Locate every blood parasite and identify its species.
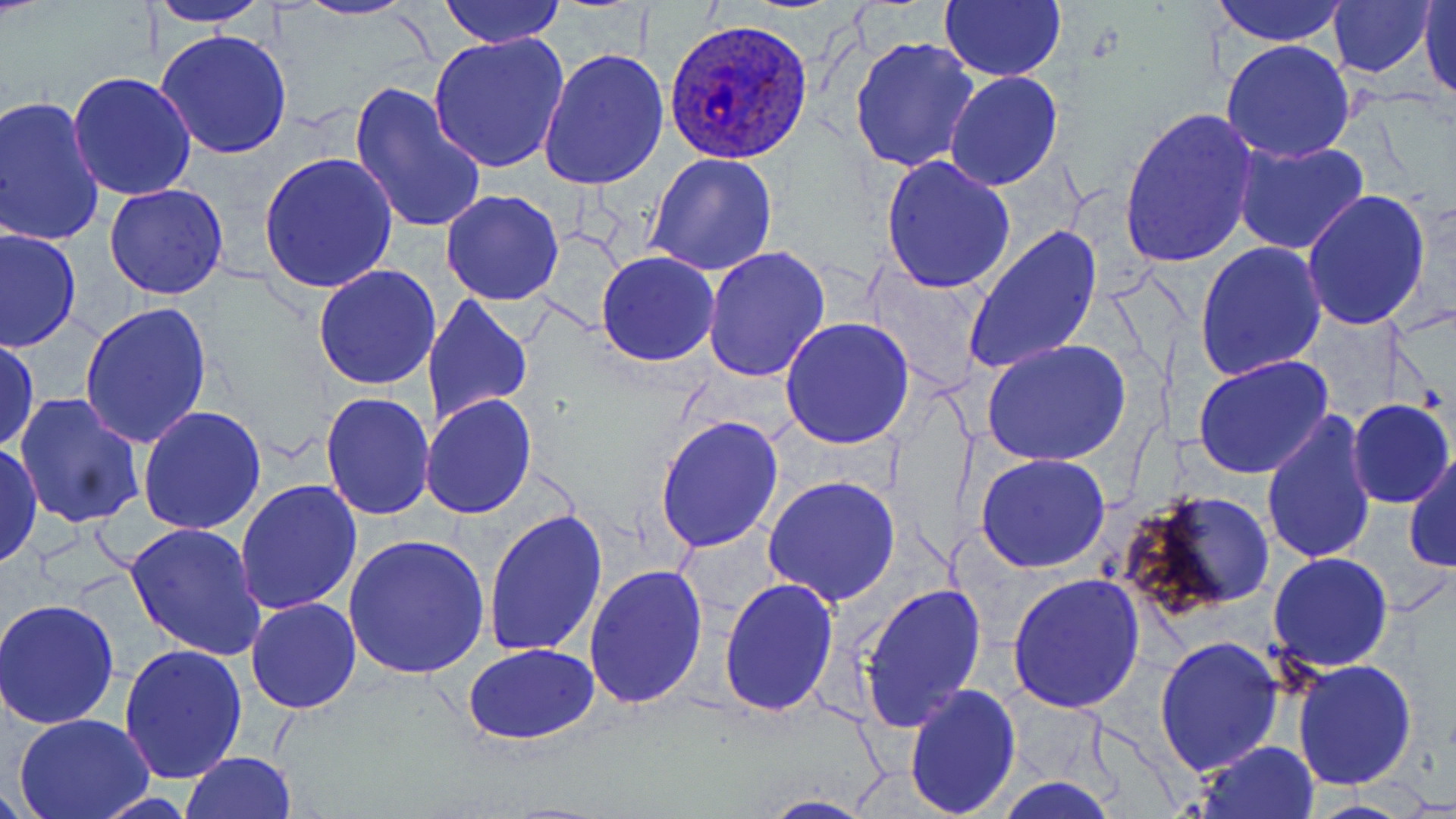

Approximate bounding boxes as named x1/y1/x2/y2 corners in pixels.
Plasmodium ovale-infected red blood cells: (x1=664, y1=21, x2=813, y2=165).
No Plasmodium falciparum, Plasmodium malariae, Plasmodium vivax, Babesia divergens, or Trypanosoma brucei observed.

slide-level diagnosis = Plasmodium ovale
modality = optical microscopy
magnification = 1000x
uninfected red blood cell locations = approximate bounding boxes as named x1/y1/x2/y2 corners in pixels: (x1=288, y1=0, x2=422, y2=21), (x1=436, y1=0, x2=569, y2=49), (x1=1208, y1=0, x2=1350, y2=48), (x1=147, y1=1, x2=272, y2=27), (x1=940, y1=2, x2=1066, y2=83), (x1=1418, y1=2, x2=1456, y2=100), (x1=1325, y1=3, x2=1438, y2=79), (x1=156, y1=29, x2=292, y2=159), (x1=429, y1=34, x2=569, y2=173), (x1=850, y1=36, x2=977, y2=175), (x1=1221, y1=41, x2=1355, y2=163), (x1=541, y1=48, x2=668, y2=191), (x1=945, y1=70, x2=1063, y2=192), (x1=69, y1=72, x2=197, y2=201), (x1=350, y1=82, x2=486, y2=236), (x1=0, y1=98, x2=104, y2=247), (x1=1120, y1=107, x2=1259, y2=269), (x1=1233, y1=141, x2=1369, y2=255), (x1=260, y1=153, x2=398, y2=294), (x1=646, y1=153, x2=777, y2=277), (x1=880, y1=157, x2=1015, y2=295), (x1=105, y1=182, x2=228, y2=300), (x1=1301, y1=189, x2=1429, y2=331), (x1=442, y1=190, x2=564, y2=307), (x1=962, y1=227, x2=1101, y2=377), (x1=1, y1=229, x2=78, y2=354), (x1=1196, y1=243, x2=1327, y2=381), (x1=703, y1=248, x2=830, y2=381), (x1=597, y1=252, x2=719, y2=366), (x1=312, y1=265, x2=441, y2=392), (x1=424, y1=294, x2=532, y2=433), (x1=82, y1=305, x2=212, y2=448), (x1=780, y1=318, x2=913, y2=448), (x1=0, y1=338, x2=40, y2=451), (x1=979, y1=338, x2=1132, y2=468), (x1=1193, y1=356, x2=1334, y2=479), (x1=321, y1=392, x2=435, y2=520), (x1=14, y1=394, x2=145, y2=529), (x1=422, y1=394, x2=535, y2=518), (x1=1348, y1=399, x2=1453, y2=506), (x1=137, y1=405, x2=266, y2=536), (x1=1261, y1=409, x2=1374, y2=568), (x1=655, y1=415, x2=784, y2=556), (x1=0, y1=443, x2=44, y2=569), (x1=1406, y1=451, x2=1456, y2=575), (x1=974, y1=453, x2=1111, y2=573), (x1=762, y1=476, x2=900, y2=607), (x1=234, y1=478, x2=361, y2=618), (x1=1116, y1=486, x2=1275, y2=618), (x1=485, y1=508, x2=608, y2=660), (x1=124, y1=521, x2=265, y2=660), (x1=343, y1=535, x2=489, y2=679), (x1=1269, y1=553, x2=1393, y2=674), (x1=585, y1=565, x2=708, y2=708), (x1=1008, y1=575, x2=1145, y2=713), (x1=719, y1=578, x2=839, y2=717), (x1=855, y1=580, x2=987, y2=735), (x1=245, y1=597, x2=361, y2=715), (x1=0, y1=599, x2=120, y2=729), (x1=1156, y1=637, x2=1283, y2=775), (x1=119, y1=643, x2=247, y2=784), (x1=462, y1=643, x2=599, y2=746), (x1=1292, y1=659, x2=1416, y2=792), (x1=904, y1=684, x2=1021, y2=817), (x1=12, y1=714, x2=154, y2=818), (x1=1197, y1=740, x2=1319, y2=819), (x1=180, y1=753, x2=299, y2=819), (x1=754, y1=795, x2=881, y2=818)
preparation = thin blood film
image size = 1456×819 pixels
field of view = one of a larger specimen
stain = May-Grünwald-Giemsa